State which parasite is depicted.
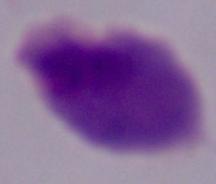
This is a trichomonad.

Summary:
  - Magnification: 1000x
  - Modality: photomicrograph